Name the blood parasite species.
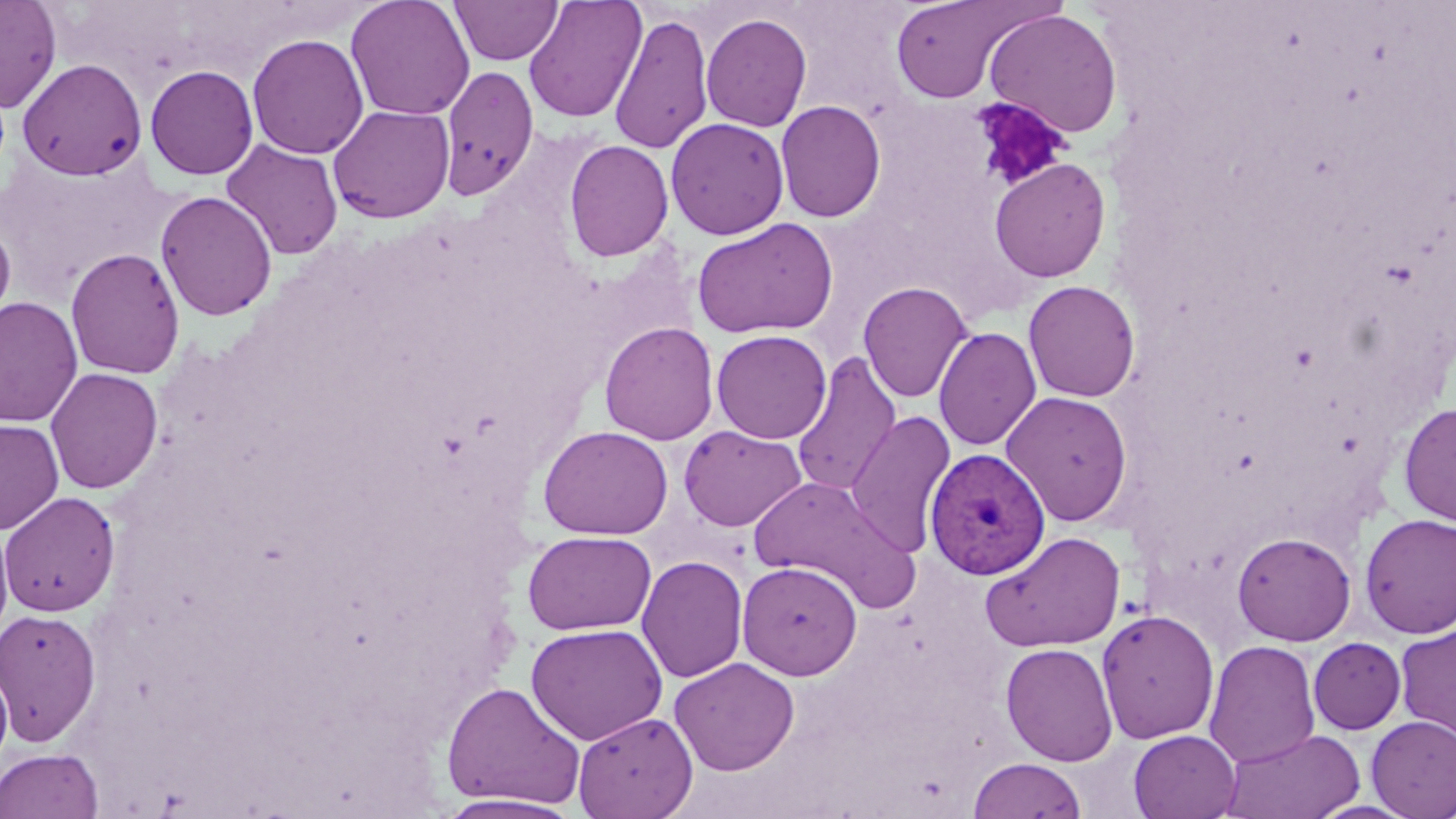
Plasmodium vivax.

field of view = single
stain = May-Grünwald-Giemsa
platelet locations = approximate bounding boxes as named x1/y1/x2/y2 corners in pixels: (x1=969, y1=98, x2=1072, y2=191)
image size = 1456×819 pixels
magnification = 1000x
Plasmodium vivax-infected red blood cell locations = approximate bounding boxes as named x1/y1/x2/y2 corners in pixels: (x1=925, y1=447, x2=1051, y2=580)
modality = optical microscopy
uninfected red blood cell locations = approximate bounding boxes as named x1/y1/x2/y2 corners in pixels: (x1=0, y1=0, x2=62, y2=112), (x1=345, y1=0, x2=475, y2=121), (x1=450, y1=0, x2=563, y2=65), (x1=889, y1=0, x2=1027, y2=103), (x1=523, y1=1, x2=647, y2=123), (x1=983, y1=8, x2=1123, y2=138), (x1=610, y1=12, x2=714, y2=154), (x1=701, y1=12, x2=812, y2=132), (x1=247, y1=33, x2=369, y2=159), (x1=17, y1=58, x2=148, y2=180), (x1=145, y1=64, x2=259, y2=180), (x1=438, y1=66, x2=539, y2=200), (x1=776, y1=100, x2=887, y2=222), (x1=328, y1=104, x2=455, y2=224), (x1=665, y1=117, x2=789, y2=240), (x1=221, y1=139, x2=343, y2=260), (x1=564, y1=139, x2=674, y2=262), (x1=989, y1=158, x2=1112, y2=282), (x1=155, y1=190, x2=277, y2=321), (x1=691, y1=217, x2=839, y2=339), (x1=1, y1=219, x2=16, y2=329), (x1=65, y1=247, x2=185, y2=380), (x1=858, y1=280, x2=974, y2=403), (x1=1023, y1=280, x2=1141, y2=402), (x1=0, y1=296, x2=83, y2=427), (x1=599, y1=322, x2=719, y2=445), (x1=933, y1=327, x2=1042, y2=451), (x1=711, y1=329, x2=831, y2=444), (x1=791, y1=353, x2=902, y2=497), (x1=45, y1=367, x2=163, y2=494), (x1=1001, y1=390, x2=1133, y2=526), (x1=1398, y1=401, x2=1456, y2=527), (x1=843, y1=411, x2=956, y2=557), (x1=0, y1=418, x2=65, y2=535), (x1=537, y1=425, x2=673, y2=540), (x1=678, y1=425, x2=807, y2=532), (x1=747, y1=475, x2=918, y2=609), (x1=0, y1=491, x2=120, y2=616), (x1=1359, y1=513, x2=1456, y2=639), (x1=0, y1=521, x2=15, y2=643), (x1=981, y1=530, x2=1126, y2=654), (x1=522, y1=531, x2=656, y2=635), (x1=1232, y1=531, x2=1356, y2=645), (x1=636, y1=555, x2=748, y2=683), (x1=737, y1=561, x2=862, y2=679), (x1=0, y1=608, x2=102, y2=747), (x1=1096, y1=609, x2=1219, y2=744), (x1=1395, y1=622, x2=1456, y2=743), (x1=526, y1=623, x2=667, y2=745), (x1=1308, y1=637, x2=1406, y2=735), (x1=1204, y1=639, x2=1320, y2=768), (x1=1000, y1=642, x2=1119, y2=766), (x1=669, y1=656, x2=800, y2=776), (x1=0, y1=658, x2=13, y2=771), (x1=440, y1=680, x2=586, y2=810), (x1=572, y1=711, x2=698, y2=819), (x1=1367, y1=716, x2=1456, y2=818), (x1=1221, y1=728, x2=1364, y2=819), (x1=1128, y1=729, x2=1241, y2=819), (x1=0, y1=747, x2=104, y2=819), (x1=967, y1=758, x2=1087, y2=818), (x1=433, y1=794, x2=586, y2=819)
preparation = thin blood film